Identify the cell.
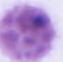
This is an erythrocyte.

Summary:
  - Modality: micrograph
  - Magnification: 1000x